Identify the parasite.
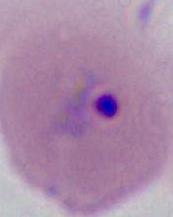
This is Plasmodium.

Micrograph. 400x or 1000x magnification.